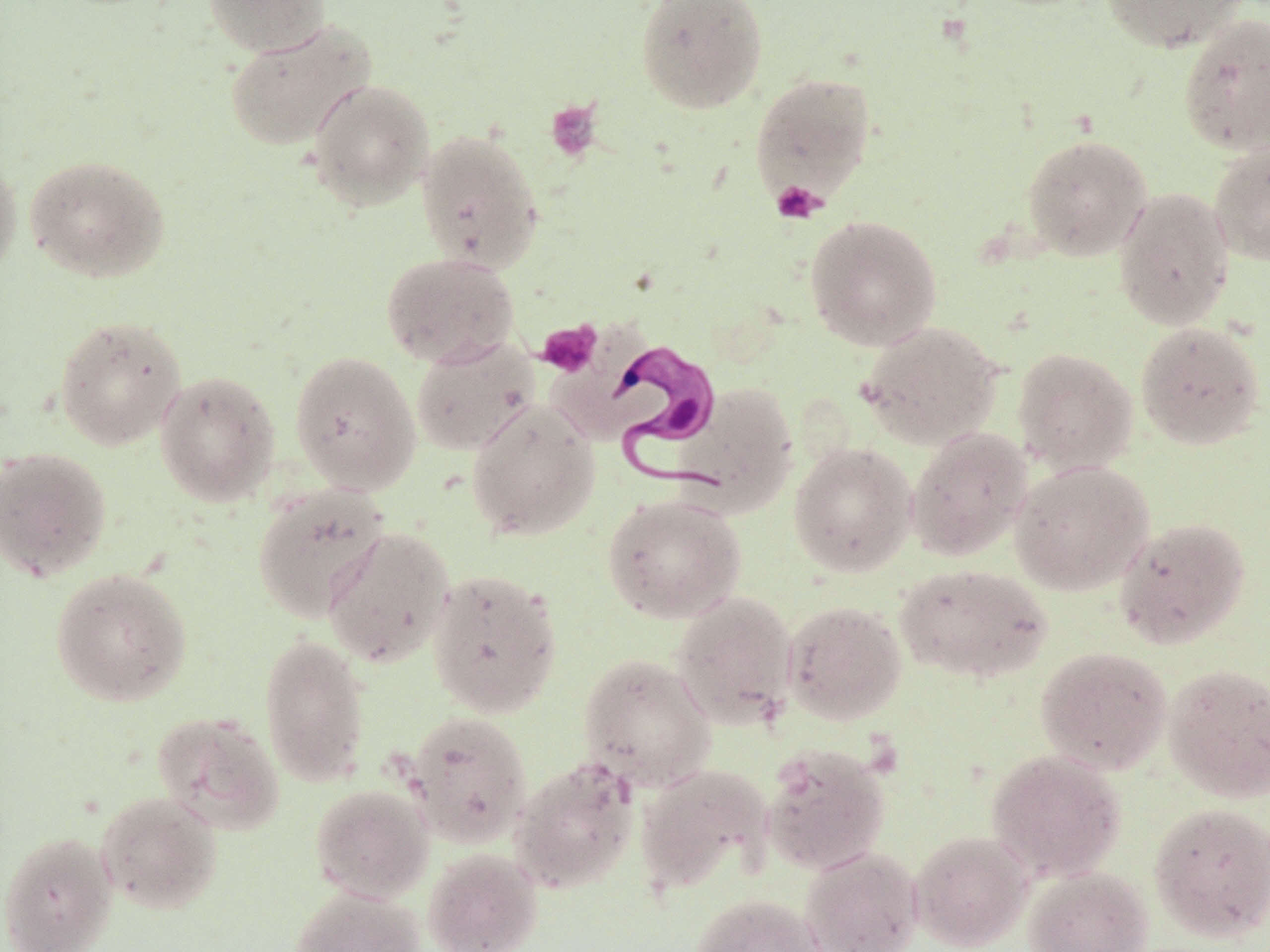

Approximate bounding boxes as (x1, y1, x2, y2) in pixels. Platelet locations: (545, 100, 603, 161), (771, 181, 825, 224), (537, 321, 601, 377). Trypanosoma brucei locations: (607, 337, 724, 494). Uninfected red blood cell locations: (203, 0, 331, 56), (635, 0, 769, 114), (1100, 0, 1251, 53), (1177, 12, 1270, 155), (224, 20, 376, 151), (749, 71, 878, 206), (306, 78, 435, 210), (415, 128, 544, 274), (1020, 133, 1152, 261), (1208, 140, 1270, 266), (0, 152, 22, 286), (24, 153, 171, 284), (1113, 186, 1235, 331), (804, 214, 943, 350), (381, 251, 519, 368), (54, 314, 187, 450), (858, 320, 1004, 449), (1135, 321, 1266, 451), (410, 336, 540, 457), (1012, 347, 1138, 475), (289, 350, 422, 495), (154, 370, 280, 507), (674, 384, 798, 516), (466, 399, 601, 541), (906, 427, 1033, 562), (788, 441, 917, 577), (0, 446, 112, 582), (1009, 460, 1155, 595), (251, 482, 389, 622), (602, 492, 746, 623), (1113, 516, 1251, 649), (322, 526, 455, 668), (894, 562, 1053, 684), (50, 567, 192, 707), (426, 568, 563, 718), (669, 590, 799, 729), (782, 600, 907, 725), (259, 633, 371, 787), (1035, 646, 1172, 774), (577, 652, 716, 791), (1163, 663, 1270, 803), (405, 710, 533, 847), (151, 711, 286, 835), (760, 742, 891, 876), (985, 749, 1125, 881), (510, 757, 640, 894), (634, 763, 774, 893), (310, 783, 434, 903), (95, 790, 223, 915), (1148, 801, 1270, 943), (909, 830, 1033, 951), (0, 831, 118, 952), (799, 846, 924, 952), (423, 848, 543, 952), (1024, 866, 1153, 952), (288, 888, 426, 952), (690, 893, 826, 952). Slide-level diagnosis: Trypanosoma brucei. Image is 1270×952 pixels. Optical microscopy. Thin blood smear. 1000x magnification. May-Grünwald-Giemsa-stained preparation. Single field of view.